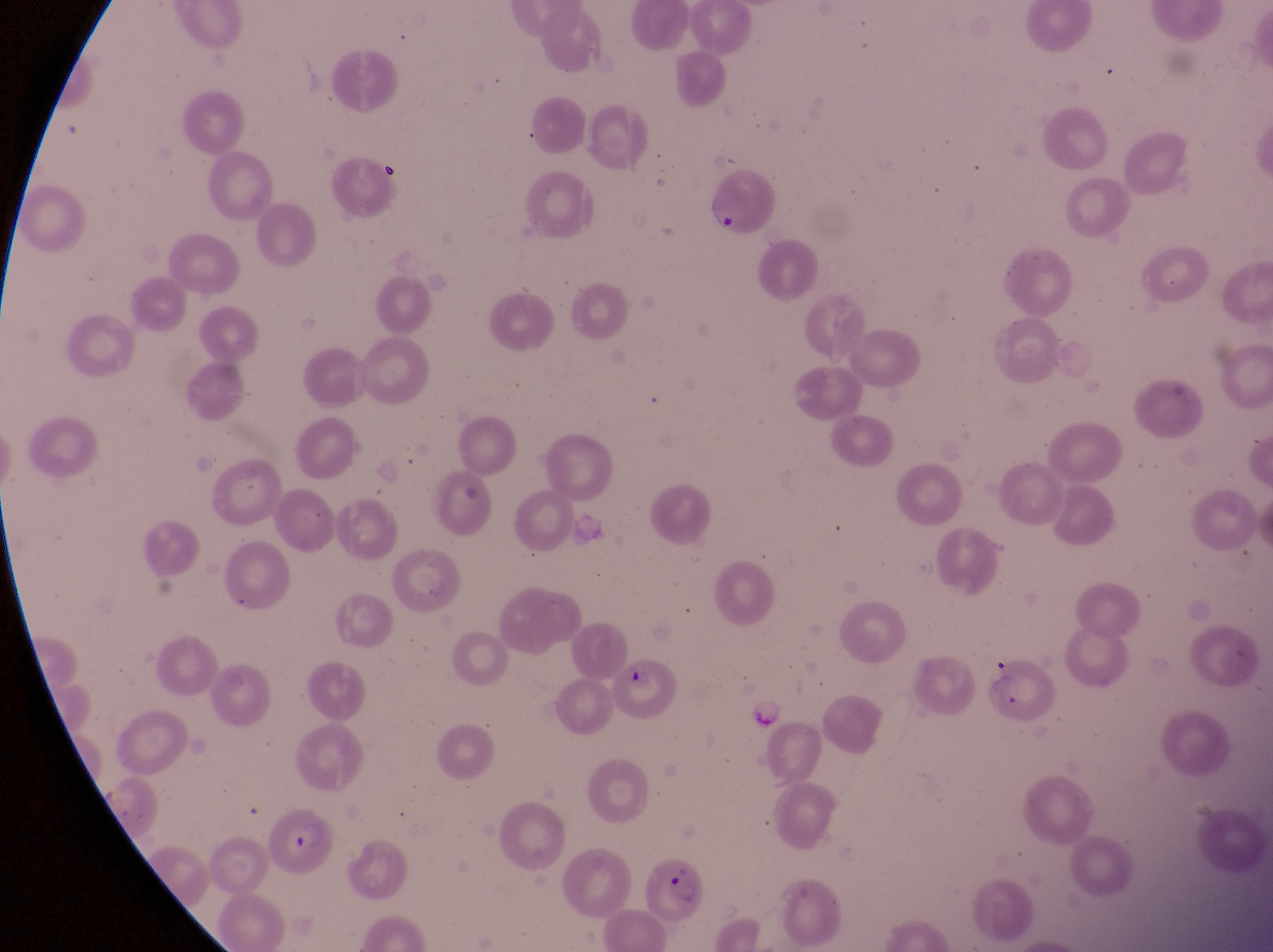 Approximate bounding boxes as [left, top, right, bottom] in pixels. Artifact (platelet-like body, stain precipitate, or debris) locations: [377, 158, 419, 190], [746, 697, 788, 730]. Parasitised red blood cell locations: [612, 657, 681, 732], [991, 663, 1054, 725], [267, 816, 336, 883], [632, 851, 706, 929]. Collected in Uganda. Photographed through the eyepiece of an Olympus CX-23 microscope with a smartphone camera. Image is 1273×952 pixels. One field of view. Magnification of 1000x. Thin blood film.